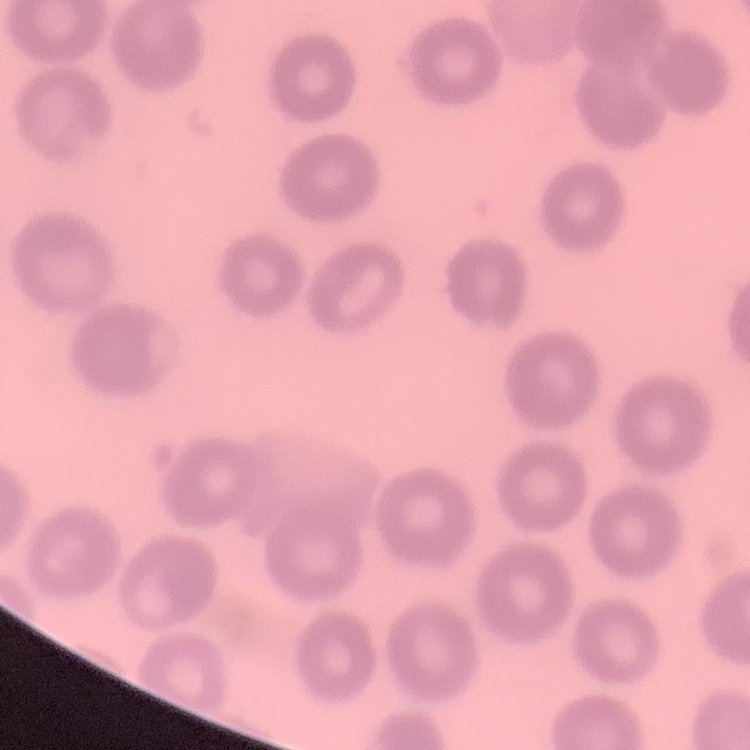

{
  "red_blood_cell_morphology": "no rouleaux formation",
  "image_type": "one tile cut from a larger photomicrograph",
  "stain": "Field's or Giemsa",
  "preparation": "thin peripheral smear"
}